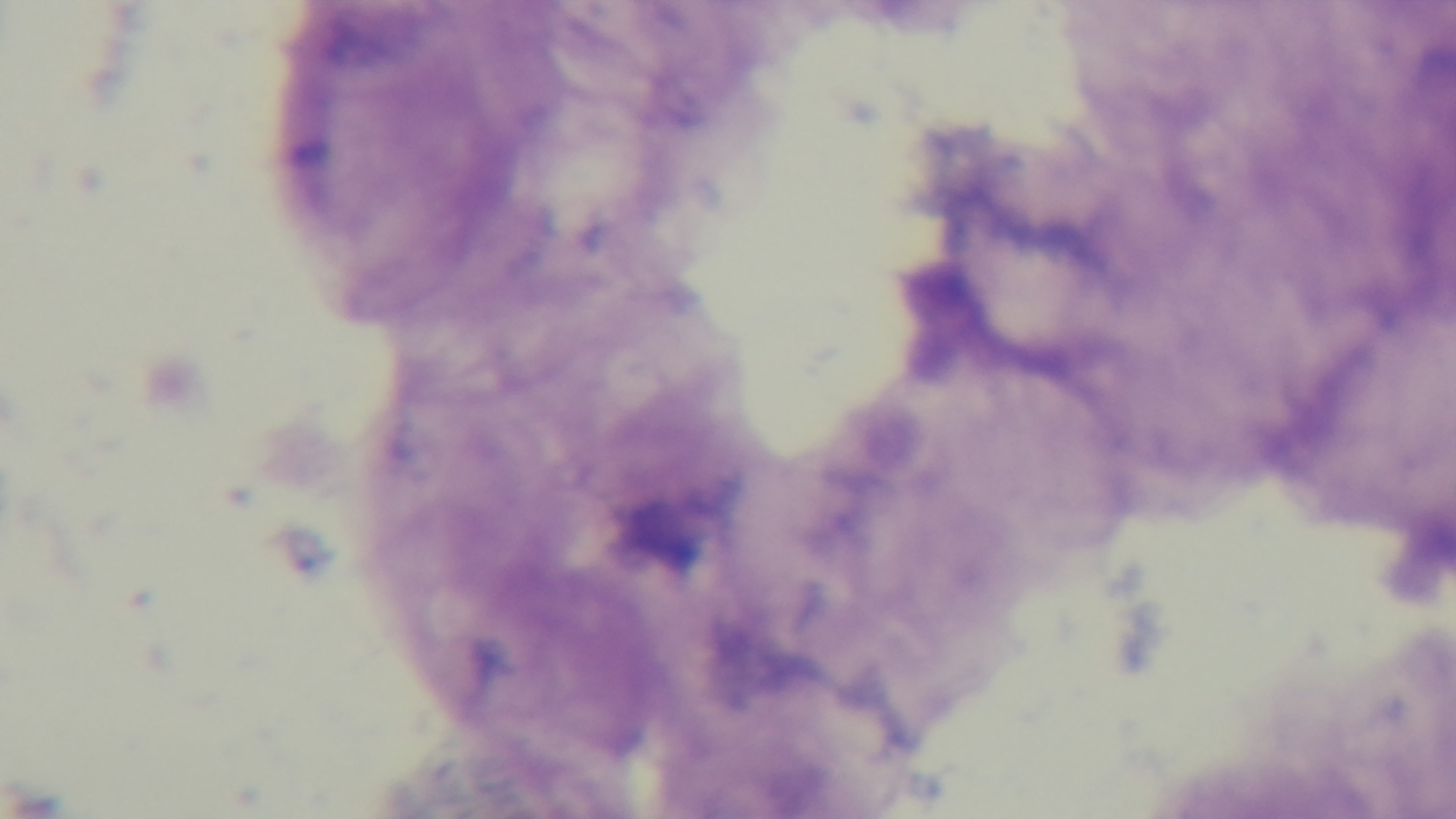
Preparation: thick blood film. Giemsa stain. Light microscopy. Single field of view. Malaria status: uninfected. 100x oil-immersion objective. Captured with a mounted 4K digital camera.